Classify this cell by malaria status.
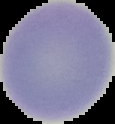

It is uninfected.

Image is 115×124 pixels. Segmented cell region on a black background. From a thin blood film.